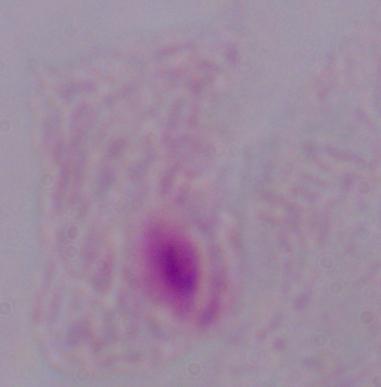

magnification = 1000x
identification = trichomonad
modality = micrograph